State which parasite is depicted.
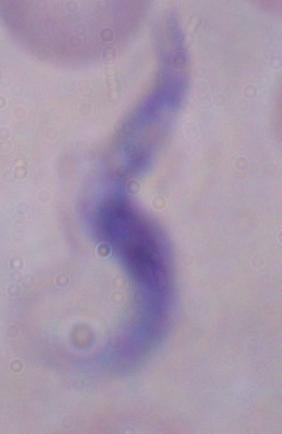
This is a trypanosome.

Summary:
  - Modality: photomicrograph
  - Magnification: 1000x